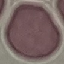
malaria status = uninfected
capture = smartphone through the microscope eyepiece
preparation = thin blood film
image type = automatically extracted cell patch, resized to 64 × 64 pixels
stain = Giemsa